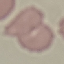

Result: negative for malaria parasites. Thin smear of blood. Giemsa-stained preparation. Cell patch, automatically extracted from a larger field of view and resized to 64 × 64 pixels. Photographed with a smartphone camera at the microscope eyepiece.